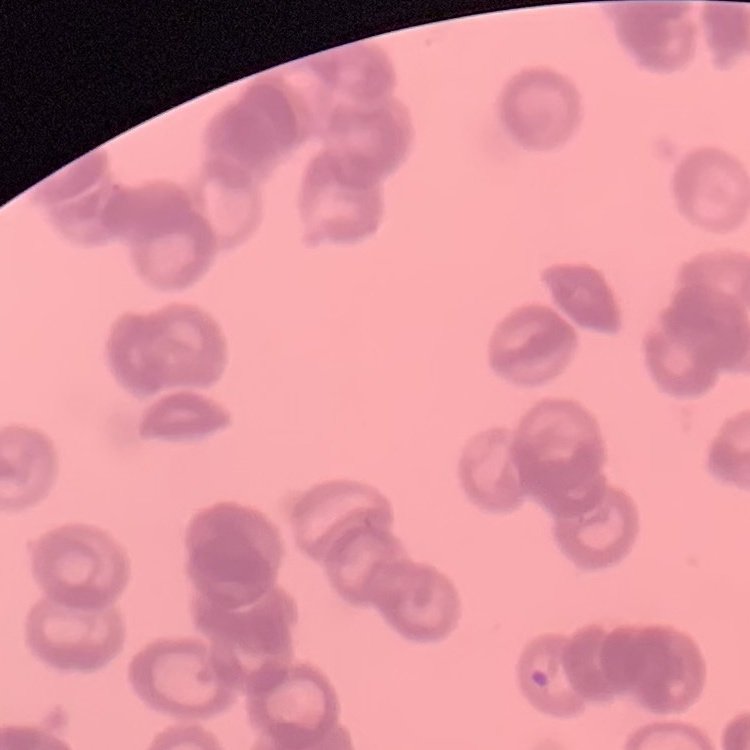 The red blood cells exhibit rouleaux formation. Stained with either Field's or Giemsa. One tile cut from a larger photomicrograph. Thin peripheral smear.